Assess this cell for malaria.
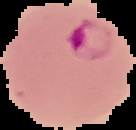

Parasitized.

Summary:
  - Image size: 136×130 pixels
  - Image type: segmented cell region on a black background
  - Preparation: thin blood smear